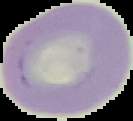

Summary:
  - Image size: 133×121 pixels
  - Preparation: thin blood smear
  - Result: no Plasmodium parasites seen
  - Image type: segmented cell region on a black background